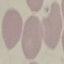
Summary:
  - Result: no malaria parasites detected
  - Stain: Giemsa
  - Capture: smartphone through the microscope eyepiece
  - Preparation: thin blood film
  - Image type: cell patch, automatically extracted from a larger field of view and resized to 64 × 64 pixels